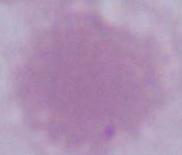

{
  "identification": "erythrocyte",
  "magnification": "1000x",
  "modality": "micrograph"
}